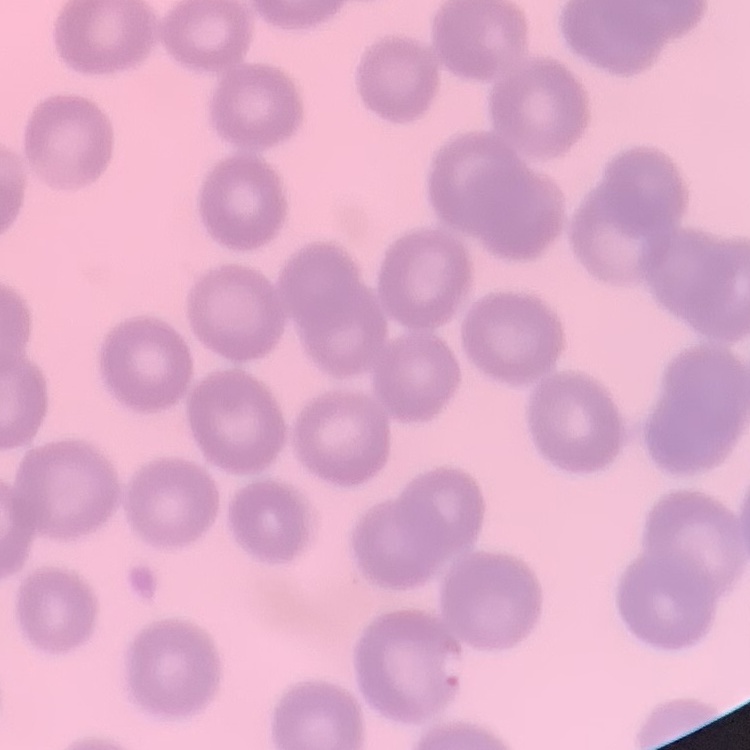

Summary:
  - Erythrocyte morphology: no rouleaux formation
  - Image type: square crop of a larger photomicrograph
  - Preparation: thin peripheral smear
  - Stain: Field's or Giemsa